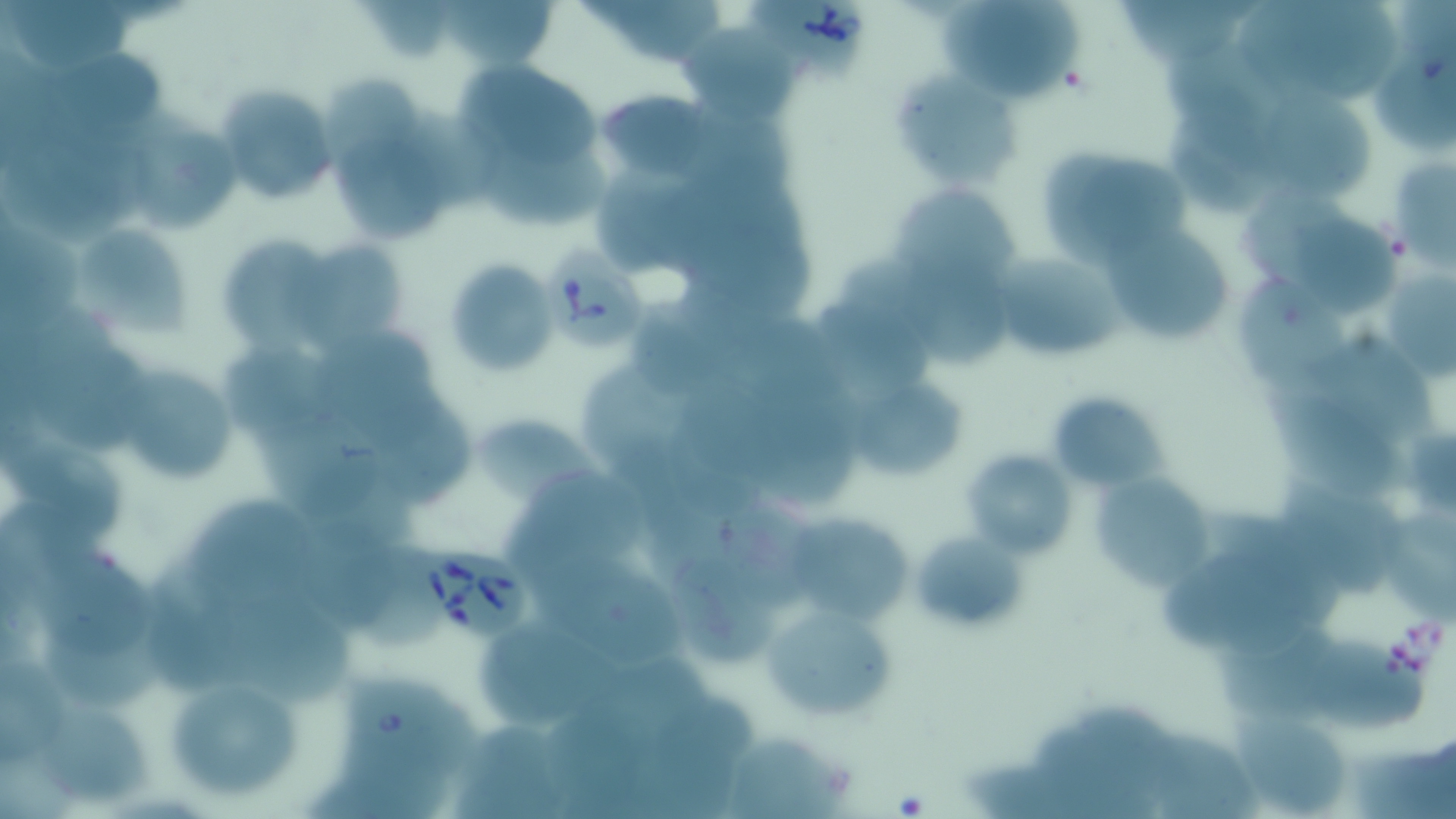
Summary:
  - Coordinate format: approximate bounding boxes as named x1/y1/x2/y2 corners in pixels
  - Uninfected red blood cell locations: (x1=7, y1=0, x2=132, y2=70), (x1=935, y1=0, x2=1087, y2=105), (x1=1119, y1=0, x2=1245, y2=66), (x1=440, y1=1, x2=564, y2=69), (x1=607, y1=1, x2=731, y2=67), (x1=367, y1=2, x2=449, y2=62), (x1=1313, y1=2, x2=1404, y2=100), (x1=1236, y1=3, x2=1354, y2=99), (x1=687, y1=27, x2=802, y2=121), (x1=1162, y1=27, x2=1287, y2=109), (x1=1377, y1=45, x2=1456, y2=158), (x1=454, y1=47, x2=604, y2=167), (x1=52, y1=56, x2=175, y2=131), (x1=898, y1=70, x2=1023, y2=193), (x1=322, y1=74, x2=422, y2=171), (x1=1246, y1=79, x2=1379, y2=200), (x1=215, y1=83, x2=341, y2=208), (x1=595, y1=87, x2=717, y2=185), (x1=1166, y1=101, x2=1286, y2=214), (x1=687, y1=104, x2=801, y2=201), (x1=141, y1=118, x2=249, y2=236), (x1=332, y1=132, x2=442, y2=244), (x1=1036, y1=142, x2=1191, y2=266), (x1=17, y1=144, x2=127, y2=244), (x1=472, y1=144, x2=610, y2=226), (x1=1388, y1=156, x2=1455, y2=267), (x1=598, y1=170, x2=715, y2=269), (x1=897, y1=181, x2=1025, y2=287), (x1=1235, y1=185, x2=1358, y2=287), (x1=1294, y1=207, x2=1407, y2=319), (x1=79, y1=220, x2=193, y2=335), (x1=687, y1=222, x2=818, y2=324), (x1=1106, y1=224, x2=1227, y2=339), (x1=0, y1=229, x2=80, y2=340), (x1=223, y1=235, x2=330, y2=357), (x1=291, y1=238, x2=403, y2=358), (x1=843, y1=249, x2=1005, y2=369), (x1=988, y1=250, x2=1129, y2=363), (x1=442, y1=258, x2=558, y2=379), (x1=1242, y1=271, x2=1364, y2=410), (x1=1388, y1=273, x2=1456, y2=386), (x1=809, y1=293, x2=935, y2=396), (x1=633, y1=296, x2=742, y2=396), (x1=728, y1=308, x2=836, y2=403), (x1=319, y1=329, x2=434, y2=424), (x1=1305, y1=335, x2=1441, y2=443), (x1=38, y1=341, x2=151, y2=455), (x1=225, y1=342, x2=347, y2=427), (x1=113, y1=365, x2=233, y2=486), (x1=585, y1=369, x2=698, y2=464), (x1=856, y1=374, x2=974, y2=489), (x1=758, y1=375, x2=856, y2=507), (x1=693, y1=377, x2=804, y2=484), (x1=1263, y1=383, x2=1412, y2=504), (x1=1045, y1=391, x2=1167, y2=492), (x1=384, y1=399, x2=478, y2=510), (x1=474, y1=405, x2=606, y2=506), (x1=244, y1=409, x2=391, y2=522), (x1=8, y1=432, x2=122, y2=531), (x1=1410, y1=432, x2=1456, y2=511), (x1=959, y1=448, x2=1078, y2=560), (x1=622, y1=454, x2=730, y2=581), (x1=1090, y1=472, x2=1214, y2=593), (x1=1276, y1=473, x2=1401, y2=590), (x1=501, y1=476, x2=652, y2=580), (x1=192, y1=499, x2=314, y2=604), (x1=794, y1=512, x2=918, y2=632), (x1=303, y1=513, x2=414, y2=634), (x1=1379, y1=514, x2=1456, y2=628), (x1=721, y1=515, x2=818, y2=612), (x1=908, y1=527, x2=1033, y2=638), (x1=36, y1=543, x2=156, y2=663), (x1=1156, y1=547, x2=1332, y2=665), (x1=535, y1=557, x2=691, y2=668), (x1=677, y1=561, x2=781, y2=663), (x1=150, y1=567, x2=259, y2=688), (x1=758, y1=598, x2=899, y2=727), (x1=231, y1=599, x2=352, y2=706), (x1=466, y1=623, x2=633, y2=729), (x1=45, y1=624, x2=171, y2=709), (x1=1220, y1=626, x2=1349, y2=724), (x1=1297, y1=629, x2=1431, y2=728), (x1=610, y1=645, x2=713, y2=736), (x1=0, y1=656, x2=66, y2=765), (x1=159, y1=668, x2=311, y2=806), (x1=652, y1=696, x2=762, y2=775), (x1=45, y1=700, x2=148, y2=806), (x1=554, y1=705, x2=657, y2=809), (x1=1082, y1=707, x2=1203, y2=807), (x1=1231, y1=710, x2=1355, y2=816), (x1=455, y1=726, x2=566, y2=819), (x1=730, y1=728, x2=855, y2=816), (x1=1153, y1=734, x2=1260, y2=819), (x1=1354, y1=740, x2=1456, y2=819), (x1=314, y1=754, x2=454, y2=819), (x1=965, y1=759, x2=1122, y2=819)
  - Babesia divergens-infected red blood cell locations: (x1=742, y1=1, x2=875, y2=84), (x1=546, y1=240, x2=651, y2=352), (x1=407, y1=545, x2=534, y2=644), (x1=339, y1=683, x2=464, y2=771)
  - Slide-level diagnosis: Babesia divergens
  - Image size: 1456×819 pixels
  - Stain: May-Grünwald-Giemsa
  - Field of view: single
  - Magnification: 1000x
  - Modality: light microscopy
  - Preparation: thin blood film